Assess this cell for malaria.
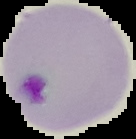
It is parasitized.

From a thin blood film. The area outside the segmented cell region is set to black. Image is 136×139 pixels.